Locate every leukocyte (white blood cell).
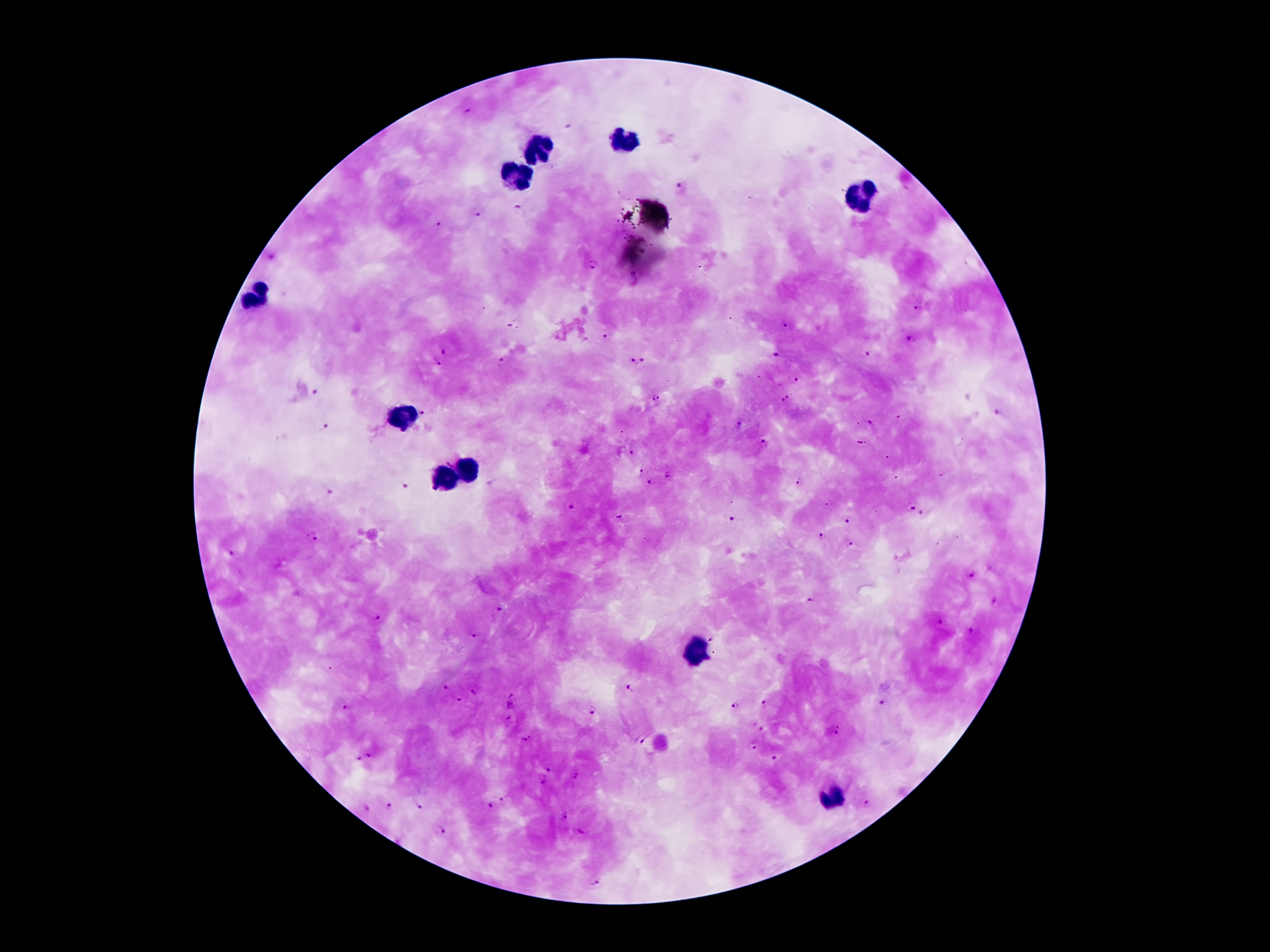
Approximate centers as (x, y) in pixels.
Leukocytes: (625, 138), (541, 148), (517, 172), (863, 198), (259, 293), (401, 415), (464, 469), (444, 479), (695, 650), (831, 801).

malaria parasite locations = (467, 111), (680, 186), (520, 207), (477, 216), (439, 225), (272, 258), (593, 265), (916, 309), (510, 325), (784, 325), (606, 336), (909, 339), (444, 352), (868, 354), (775, 355), (642, 359), (632, 360), (501, 361), (436, 363), (794, 380), (314, 393), (788, 396), (655, 399), (783, 402), (425, 412), (997, 414), (870, 423), (738, 426), (326, 428), (764, 444), (630, 455), (644, 471), (667, 475), (799, 483), (649, 484), (404, 487), (331, 491), (910, 506), (571, 507), (922, 516), (730, 518), (621, 519), (849, 519), (312, 537), (821, 537), (851, 545), (231, 554), (971, 576), (807, 600), (995, 600), (499, 610), (376, 618), (939, 623), (971, 631), (475, 635), (712, 640), (443, 687), (629, 687), (475, 691), (459, 700), (882, 703), (764, 705), (734, 706), (345, 707), (592, 711), (510, 721), (762, 728), (839, 731), (525, 739), (640, 741), (753, 745), (370, 756), (357, 759), (774, 759), (548, 769), (576, 775), (543, 781), (500, 799), (867, 802), (390, 806), (419, 806), (489, 806), (367, 809), (564, 817), (442, 833), (597, 883)
capture = smartphone camera through the microscope eyepiece
magnification = 100x
preparation = thick blood film
stain = Giemsa
image size = 1270×952 pixels
field of view = one from this slide
patient malaria status = positive for Plasmodium falciparum